Report the malaria status of this cell.
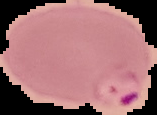

Parasitized.

image size = 157×115 pixels
image type = segmented cell region on a black background
preparation = thin blood smear